Locate platelets.
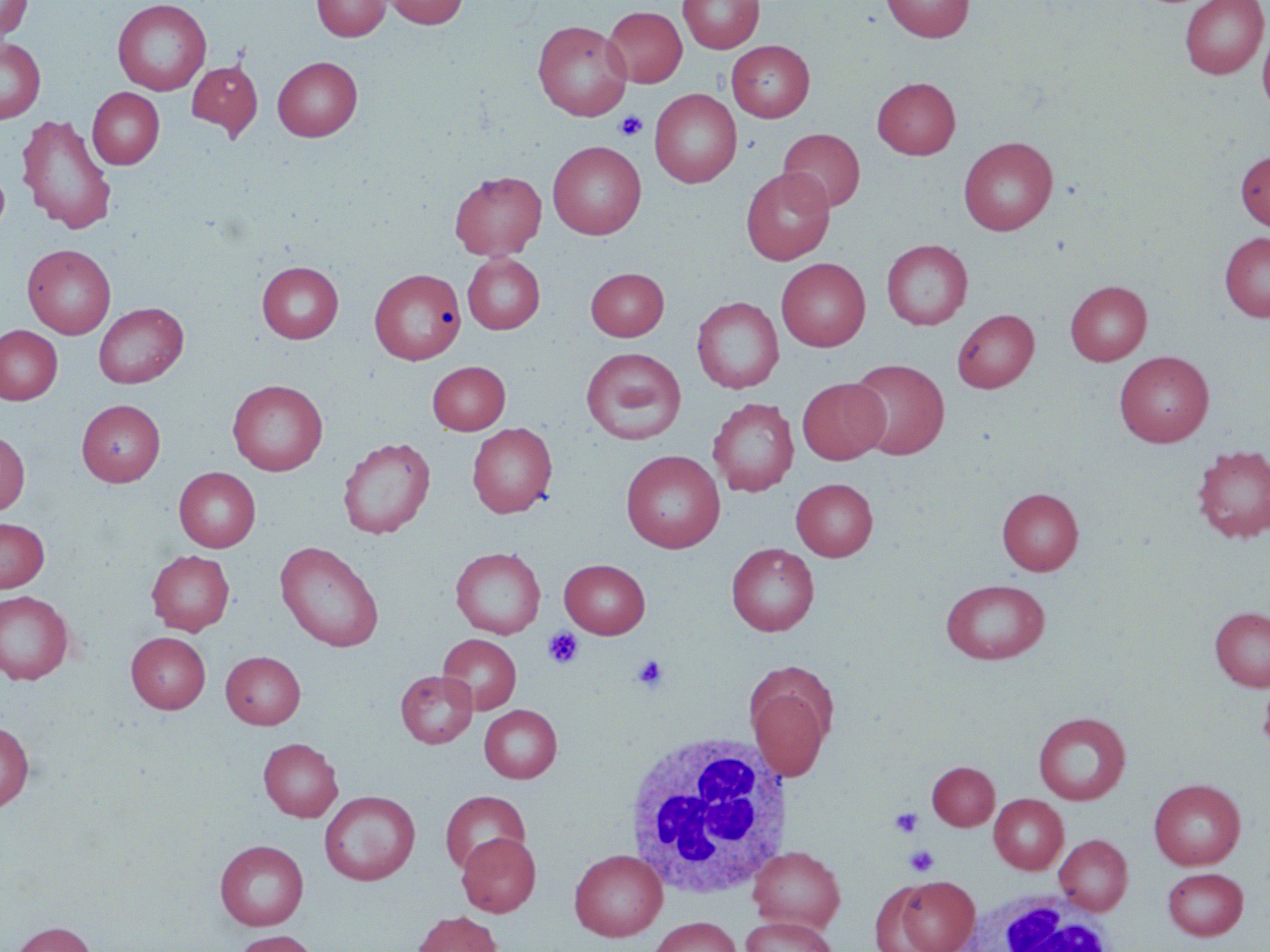
Approximate bounding boxes as (x1,y1)-(x2,y2) corner pairs in pixels.
Platelets: (614,111)-(648,140), (543,628)-(584,669), (631,654)-(669,693), (889,808)-(924,837), (904,845)-(939,876).

Uninfected red blood cell locations: (0,0)-(33,42), (112,0)-(212,95), (312,0)-(390,41), (381,0)-(468,29), (678,0)-(763,53), (881,0)-(975,42), (1180,0)-(1268,79), (602,6)-(687,87), (532,20)-(632,121), (1257,26)-(1270,116), (0,37)-(45,123), (726,40)-(815,122), (272,56)-(362,141), (187,59)-(263,139), (872,77)-(961,159), (88,88)-(164,169), (649,88)-(742,188), (16,113)-(116,235), (778,128)-(865,213), (958,137)-(1058,235), (548,141)-(646,240), (1235,151)-(1270,229), (0,163)-(10,238), (740,168)-(834,265), (450,171)-(546,260), (1219,232)-(1270,322), (881,239)-(972,329), (22,244)-(115,338), (462,253)-(545,334), (776,258)-(870,351), (257,261)-(343,343), (369,268)-(466,364), (585,268)-(669,340), (1065,280)-(1152,365), (692,296)-(783,393), (93,302)-(188,388), (952,308)-(1039,392), (0,325)-(63,404), (581,347)-(686,444), (1115,350)-(1214,446), (848,358)-(949,460), (427,361)-(510,434), (797,378)-(889,464), (228,379)-(328,475), (707,398)-(799,496), (76,399)-(165,486), (467,422)-(557,518), (0,431)-(30,515), (337,437)-(435,539), (1192,444)-(1270,543), (621,450)-(725,553), (174,467)-(261,552), (791,478)-(878,561), (997,487)-(1083,575), (0,517)-(49,592), (275,541)-(384,652), (726,543)-(819,636), (450,547)-(545,638), (146,550)-(235,634), (559,559)-(650,638), (940,578)-(1050,664), (0,591)-(74,685), (1210,606)-(1270,691), (126,632)-(211,713), (438,634)-(521,714), (221,651)-(305,728), (746,669)-(834,781), (396,670)-(476,748), (1258,677)-(1270,761), (480,705)-(562,782), (1033,711)-(1131,805), (0,721)-(34,811), (259,738)-(343,821), (927,761)-(999,830), (1149,779)-(1245,869), (320,790)-(420,885), (440,790)-(530,874), (990,794)-(1068,874), (456,832)-(541,917), (1055,834)-(1132,915), (215,839)-(309,930), (748,846)-(845,933), (569,849)-(667,941), (1162,867)-(1248,940), (887,875)-(980,952), (411,911)-(503,952), (741,915)-(835,952), (648,917)-(743,952), (9,921)-(97,952), (231,930)-(319,952). White blood cell locations: (622,731)-(791,900), (958,889)-(1117,952). Slide-level diagnosis: negative for blood parasites. 1000x magnification. May-Grünwald-Giemsa-stained preparation. Optical microscopy. Image is 1270×952 pixels. Thin blood smear. One field of a larger specimen.